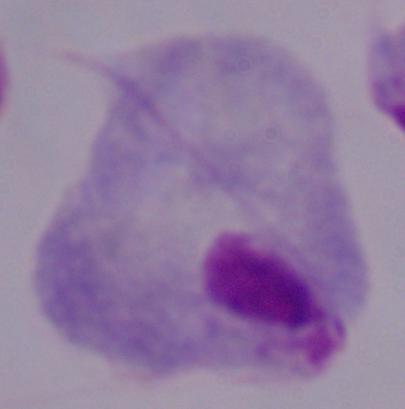

identification = trichomonad
modality = micrograph
magnification = 1000x